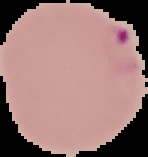 Image is 148×157 pixels. Malaria status: parasitized. Segmented cell region on a black background. From a thin blood smear.